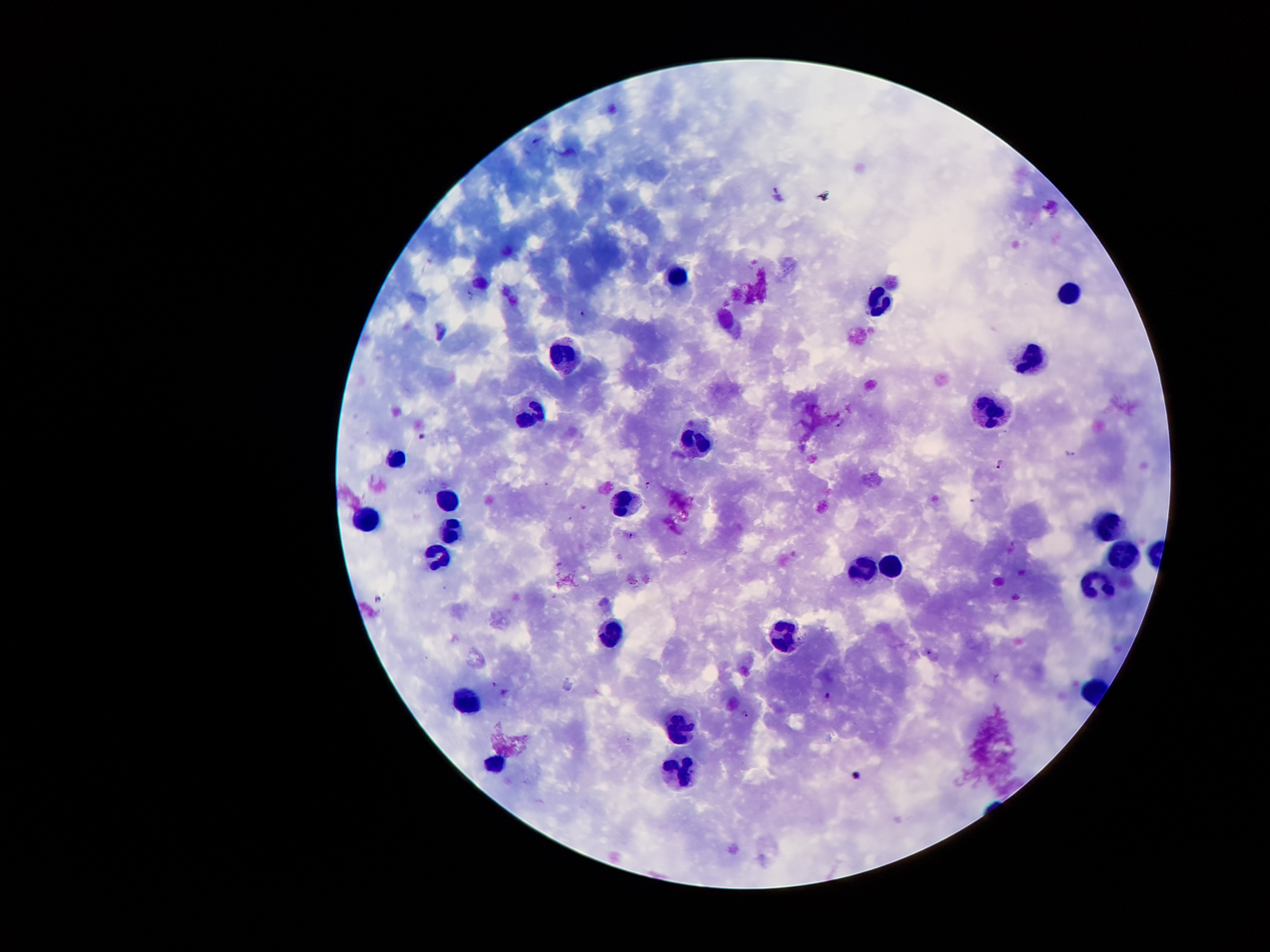

{
  "magnification": "100x",
  "field_of_view": "one from this slide",
  "preparation": "thick peripheral-blood smear",
  "plasmodium_parasite_locations": "approximate centers as (x, y) in pixels: (535, 139), (776, 189), (470, 295), (584, 313), (841, 422), (422, 435), (1070, 454), (1000, 464), (648, 485), (973, 500), (632, 534), (378, 599), (929, 653), (494, 683), (505, 692), (827, 696), (744, 713), (857, 775)",
  "leukocyte_locations": "approximate centers as (x, y) in pixels: (677, 277), (1069, 293), (877, 300), (568, 354), (1034, 357), (991, 411), (530, 420), (699, 440), (397, 460), (450, 500), (622, 504), (368, 523), (1108, 525), (453, 530), (441, 557), (1126, 557), (891, 567), (861, 571), (1098, 590), (613, 632), (784, 633), (470, 700), (682, 725), (497, 762), (682, 773)",
  "image_size": "1270×952 pixels",
  "stain": "Giemsa",
  "capture": "smartphone through the microscope eyepiece",
  "patient_malaria_status": "positive for Plasmodium falciparum"
}